State which parasite is depicted.
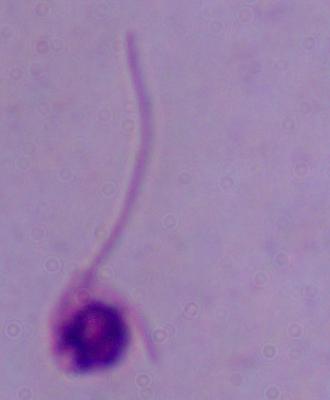
Leishmania.

modality = micrograph
magnification = 1000x